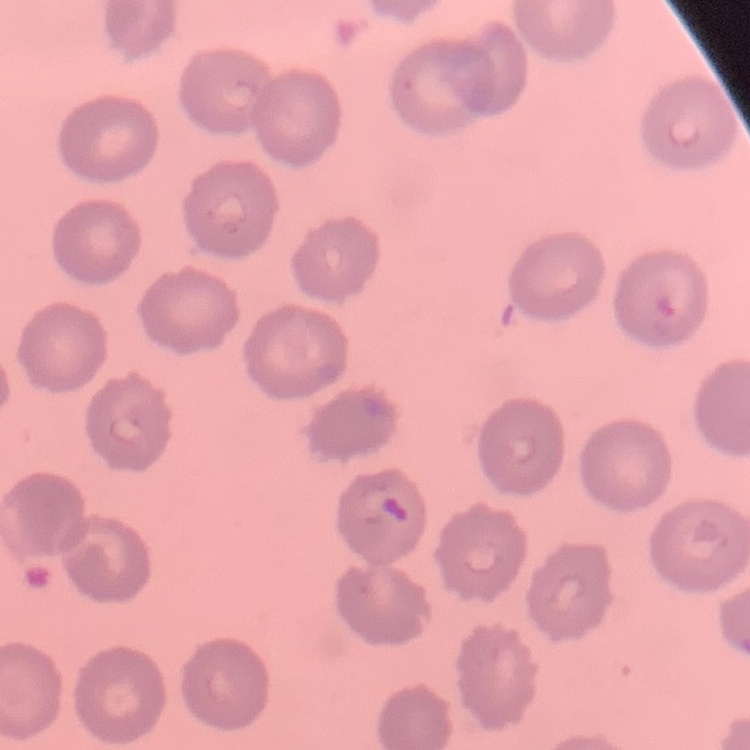
The red blood cells show no rouleaux formation. Thin peripheral smear. Stained with either Field's or Giemsa. One tile cut from a larger photomicrograph.